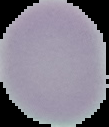 The area outside the segmented cell region is set to black. Image is 109×127 pixels. Result: negative for malaria parasites. From a thin blood film.